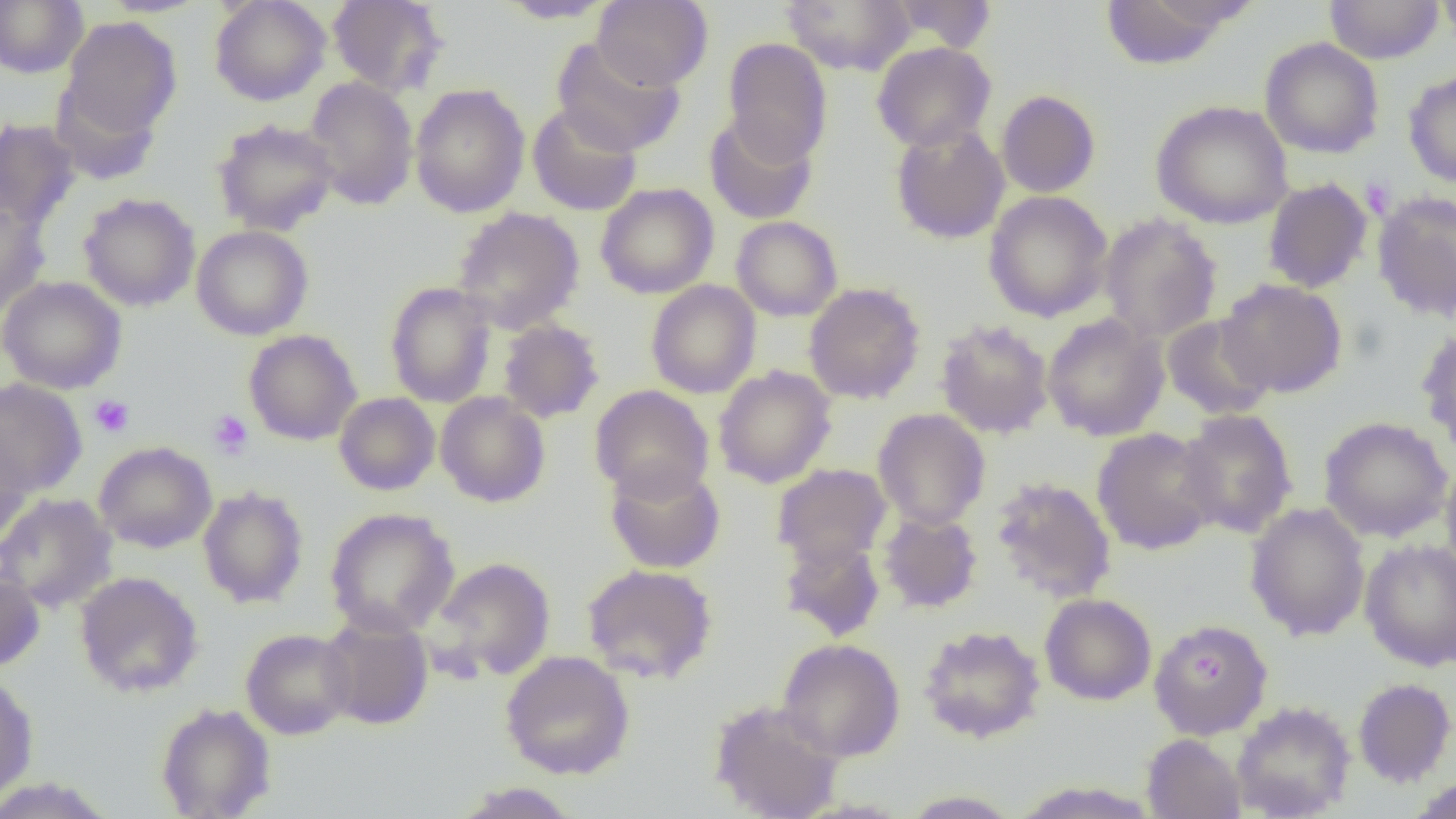
Approximate bounding boxes as named x1/y1/x2/y2 corners in pixels. Platelet locations: (x1=1361, y1=178, x2=1396, y2=220), (x1=89, y1=394, x2=135, y2=438), (x1=208, y1=410, x2=253, y2=460). Uninfected red blood cell locations: (x1=0, y1=0, x2=88, y2=78), (x1=97, y1=0, x2=211, y2=18), (x1=209, y1=0, x2=331, y2=106), (x1=327, y1=0, x2=448, y2=97), (x1=593, y1=0, x2=712, y2=91), (x1=781, y1=0, x2=916, y2=76), (x1=889, y1=0, x2=998, y2=53), (x1=1099, y1=0, x2=1244, y2=70), (x1=1324, y1=0, x2=1444, y2=64), (x1=1436, y1=0, x2=1456, y2=48), (x1=495, y1=1, x2=618, y2=23), (x1=58, y1=16, x2=182, y2=146), (x1=551, y1=36, x2=686, y2=156), (x1=722, y1=37, x2=833, y2=167), (x1=1260, y1=37, x2=1384, y2=159), (x1=871, y1=42, x2=996, y2=152), (x1=1403, y1=70, x2=1456, y2=188), (x1=303, y1=76, x2=419, y2=210), (x1=410, y1=84, x2=530, y2=218), (x1=996, y1=89, x2=1101, y2=198), (x1=1150, y1=99, x2=1293, y2=229), (x1=527, y1=103, x2=642, y2=216), (x1=704, y1=113, x2=817, y2=225), (x1=0, y1=117, x2=82, y2=231), (x1=211, y1=118, x2=339, y2=236), (x1=890, y1=122, x2=1010, y2=244), (x1=1262, y1=177, x2=1373, y2=294), (x1=595, y1=183, x2=719, y2=299), (x1=1371, y1=190, x2=1456, y2=322), (x1=983, y1=191, x2=1113, y2=322), (x1=78, y1=192, x2=200, y2=312), (x1=0, y1=200, x2=50, y2=317), (x1=451, y1=207, x2=585, y2=333), (x1=1098, y1=213, x2=1222, y2=343), (x1=731, y1=216, x2=843, y2=322), (x1=192, y1=225, x2=314, y2=340), (x1=0, y1=276, x2=126, y2=394), (x1=1217, y1=278, x2=1347, y2=398), (x1=646, y1=280, x2=761, y2=398), (x1=384, y1=281, x2=498, y2=408), (x1=804, y1=282, x2=926, y2=405), (x1=1042, y1=313, x2=1170, y2=441), (x1=1161, y1=313, x2=1276, y2=420), (x1=497, y1=319, x2=604, y2=424), (x1=935, y1=319, x2=1054, y2=439), (x1=1416, y1=324, x2=1456, y2=454), (x1=244, y1=329, x2=362, y2=446), (x1=713, y1=366, x2=837, y2=488), (x1=0, y1=378, x2=88, y2=497), (x1=589, y1=385, x2=714, y2=502), (x1=334, y1=392, x2=440, y2=496), (x1=435, y1=392, x2=551, y2=508), (x1=872, y1=408, x2=991, y2=530), (x1=1177, y1=409, x2=1298, y2=538), (x1=1319, y1=416, x2=1453, y2=543), (x1=1092, y1=428, x2=1222, y2=554), (x1=0, y1=431, x2=33, y2=552), (x1=94, y1=441, x2=217, y2=553), (x1=1440, y1=457, x2=1456, y2=581), (x1=603, y1=460, x2=726, y2=574), (x1=772, y1=463, x2=892, y2=568), (x1=990, y1=476, x2=1117, y2=603), (x1=198, y1=486, x2=309, y2=608), (x1=0, y1=493, x2=118, y2=613), (x1=1245, y1=502, x2=1370, y2=641), (x1=324, y1=507, x2=459, y2=638), (x1=878, y1=510, x2=983, y2=614), (x1=778, y1=537, x2=886, y2=642), (x1=1360, y1=538, x2=1456, y2=671), (x1=430, y1=557, x2=557, y2=681), (x1=581, y1=563, x2=718, y2=684), (x1=0, y1=564, x2=46, y2=671), (x1=75, y1=571, x2=204, y2=698), (x1=1039, y1=593, x2=1156, y2=705), (x1=319, y1=613, x2=434, y2=730), (x1=1148, y1=618, x2=1274, y2=739), (x1=919, y1=625, x2=1045, y2=743), (x1=240, y1=628, x2=356, y2=739), (x1=777, y1=638, x2=906, y2=762), (x1=500, y1=650, x2=635, y2=780), (x1=0, y1=670, x2=38, y2=804), (x1=1353, y1=677, x2=1455, y2=787), (x1=709, y1=698, x2=845, y2=819), (x1=1231, y1=700, x2=1356, y2=819), (x1=156, y1=702, x2=276, y2=818), (x1=1142, y1=734, x2=1246, y2=819), (x1=1405, y1=774, x2=1456, y2=819), (x1=0, y1=777, x2=118, y2=818), (x1=1008, y1=781, x2=1161, y2=818), (x1=450, y1=782, x2=582, y2=818), (x1=901, y1=790, x2=1022, y2=818). Slide-level diagnosis: no evidence of blood parasites. Light microscopy. Thin blood smear. One field of a larger specimen. Image is 1456×819 pixels. 1000x magnification.